Assess this cell for malaria.
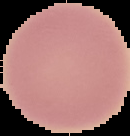
Uninfected.

Summary:
  - Image type: cell region segmented out of the field of view; surrounding area masked to black
  - Image size: 130×136 pixels
  - Preparation: thin blood film